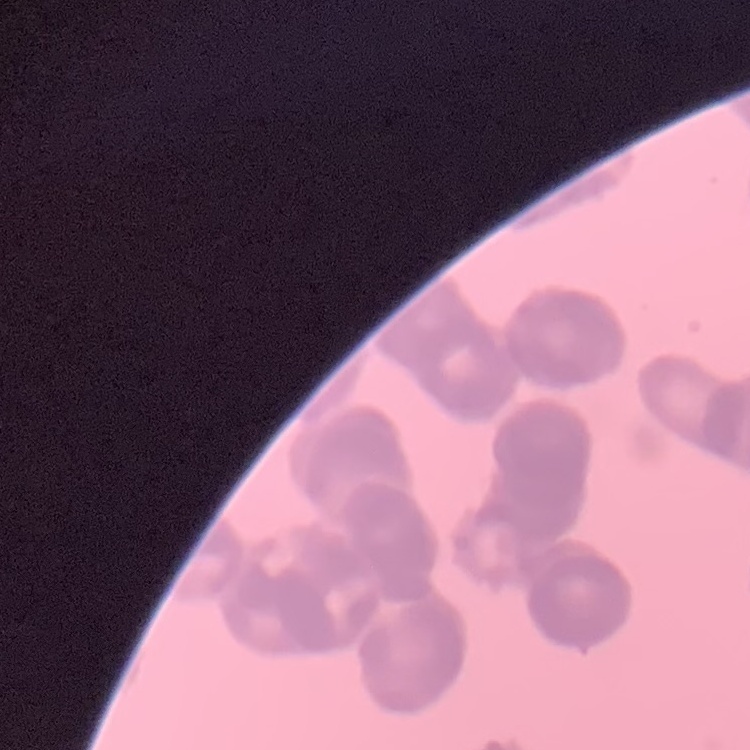
The erythrocytes exhibit rouleaux formation. One tile cut from a larger photomicrograph. Thin peripheral smear. Stained with either Field's or Giemsa.